Locate every Plasmodium parasite.
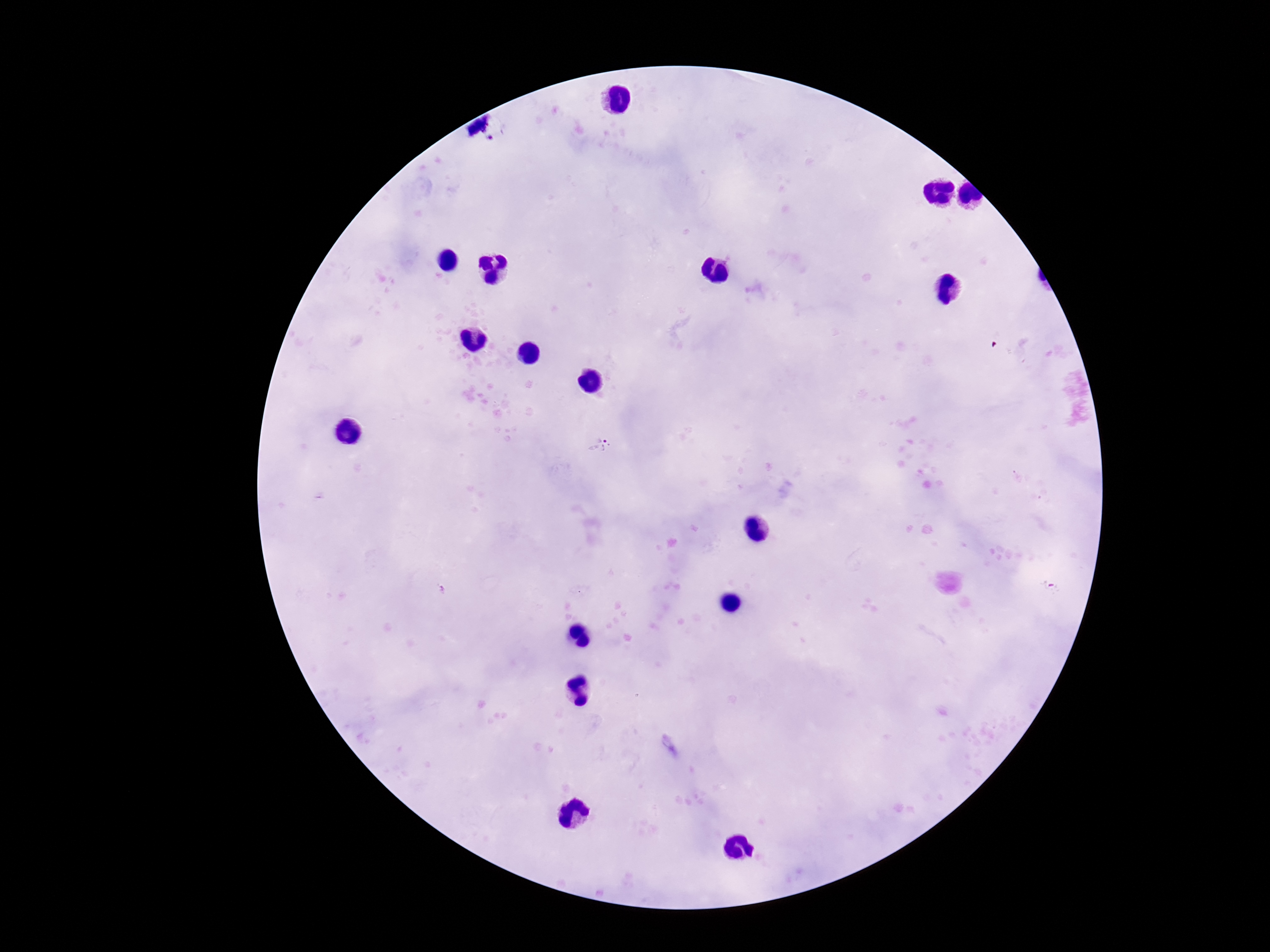

Approximate centers as [x, y] in pixels.
Plasmodium parasites: [493, 140], [599, 446], [1051, 587].

Summary:
  - Field of view: single
  - Capture: smartphone camera through the microscope eyepiece
  - Patient malaria status: infected
  - Stain: Giemsa
  - Magnification: 100x
  - Image size: 1270×952 pixels
  - Preparation: thick blood film